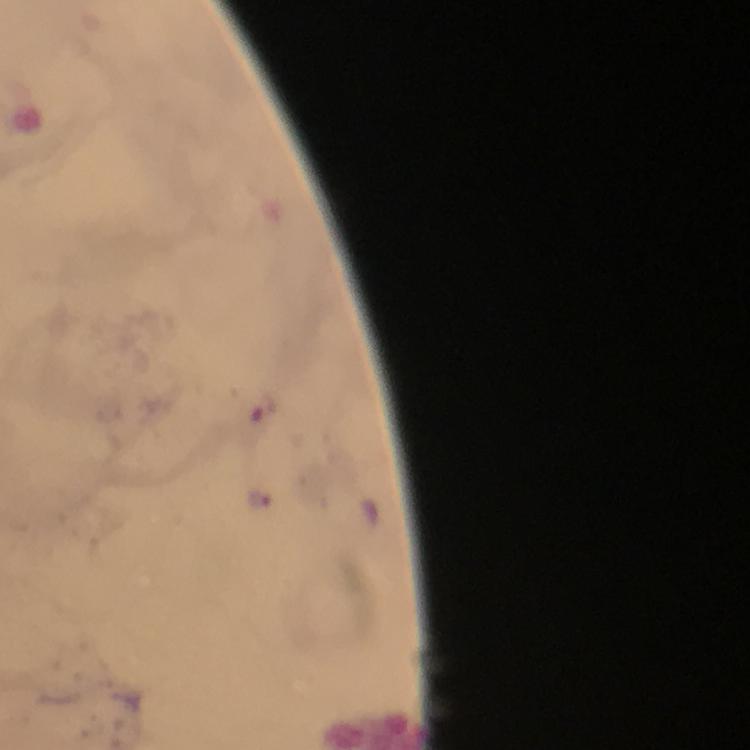

Approximate object centers, in pixels from the top-left corner. Plasmodium parasite locations: (x=259, y=498). Image is 750×750 pixels. Giemsa stain. Cropped region of a single field of view. Immersion oil was used. 100x magnification. From a diagnostic examination for malaria. Thick smear. Smartphone photograph taken through a microscope.